Locate and identify every blood parasite.
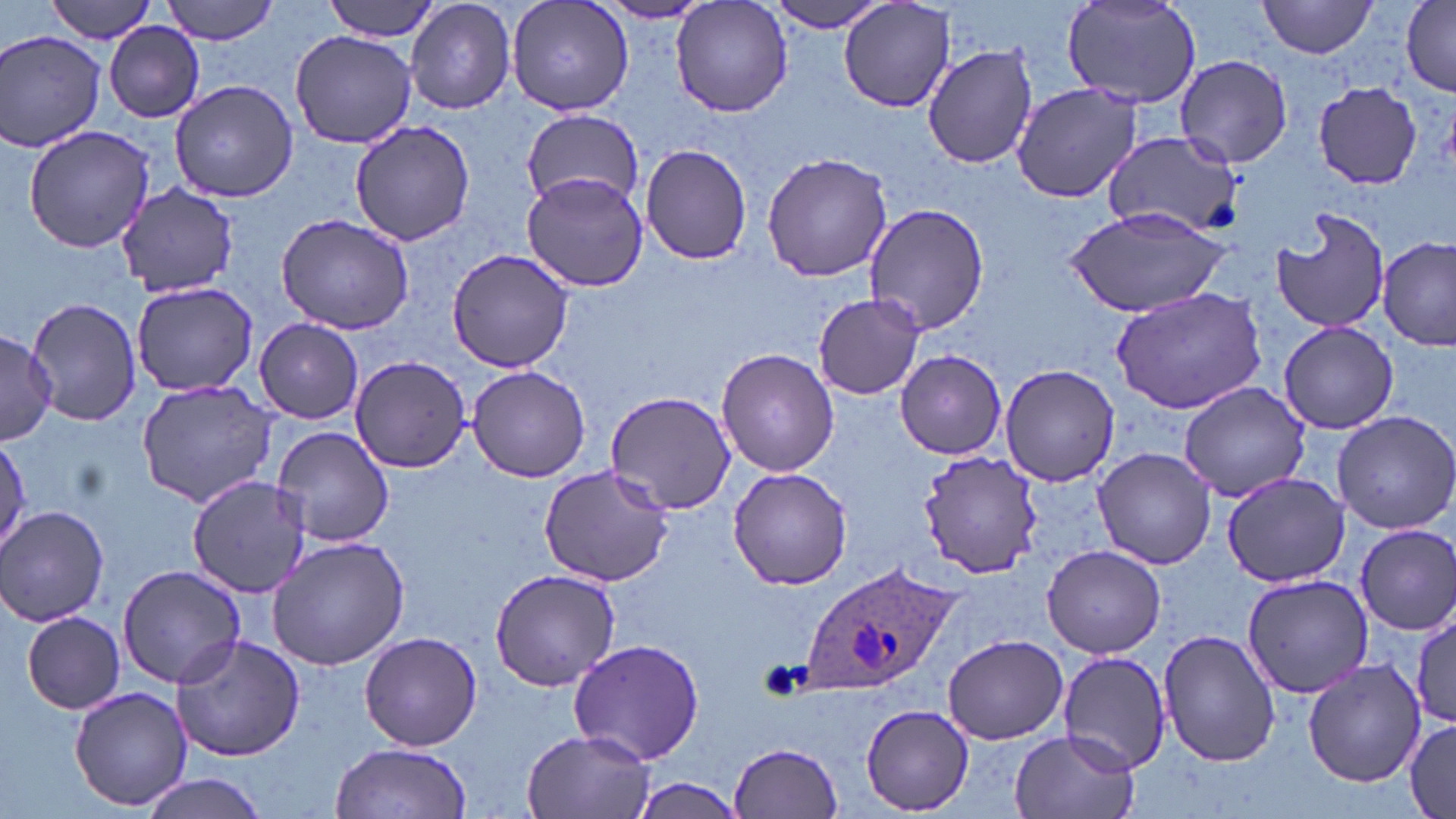
Approximate bounding boxes as named x1/y1/x2/y2 corners in pixels.
Plasmodium ovale-infected red blood cells: (x1=799, y1=560, x2=961, y2=696).
No Plasmodium falciparum, Plasmodium malariae, Plasmodium vivax, Babesia divergens, or Trypanosoma brucei observed.

Uninfected red blood cell locations: (x1=42, y1=0, x2=158, y2=42), (x1=160, y1=0, x2=284, y2=44), (x1=319, y1=0, x2=439, y2=43), (x1=507, y1=0, x2=634, y2=118), (x1=669, y1=0, x2=794, y2=119), (x1=1061, y1=0, x2=1203, y2=110), (x1=1258, y1=0, x2=1383, y2=59), (x1=406, y1=1, x2=517, y2=114), (x1=594, y1=1, x2=715, y2=23), (x1=766, y1=1, x2=889, y2=33), (x1=1401, y1=1, x2=1456, y2=94), (x1=840, y1=2, x2=958, y2=112), (x1=104, y1=21, x2=206, y2=122), (x1=290, y1=29, x2=416, y2=150), (x1=1, y1=31, x2=106, y2=154), (x1=923, y1=43, x2=1039, y2=169), (x1=1173, y1=54, x2=1293, y2=168), (x1=170, y1=78, x2=299, y2=203), (x1=1011, y1=82, x2=1141, y2=203), (x1=1314, y1=82, x2=1423, y2=189), (x1=518, y1=109, x2=646, y2=209), (x1=351, y1=120, x2=476, y2=245), (x1=23, y1=127, x2=154, y2=254), (x1=1101, y1=132, x2=1247, y2=238), (x1=641, y1=143, x2=752, y2=265), (x1=761, y1=151, x2=892, y2=282), (x1=521, y1=172, x2=650, y2=293), (x1=118, y1=184, x2=240, y2=296), (x1=864, y1=203, x2=988, y2=336), (x1=1270, y1=206, x2=1390, y2=334), (x1=1065, y1=208, x2=1234, y2=319), (x1=275, y1=212, x2=416, y2=334), (x1=1378, y1=238, x2=1455, y2=349), (x1=446, y1=247, x2=575, y2=374), (x1=130, y1=281, x2=260, y2=397), (x1=1111, y1=283, x2=1269, y2=414), (x1=814, y1=293, x2=926, y2=400), (x1=26, y1=297, x2=143, y2=429), (x1=255, y1=320, x2=364, y2=423), (x1=1278, y1=321, x2=1399, y2=435), (x1=0, y1=331, x2=55, y2=443), (x1=717, y1=349, x2=839, y2=476), (x1=895, y1=351, x2=1006, y2=459), (x1=349, y1=355, x2=473, y2=473), (x1=466, y1=364, x2=591, y2=483), (x1=1000, y1=364, x2=1120, y2=486), (x1=136, y1=380, x2=276, y2=506), (x1=1178, y1=382, x2=1312, y2=499), (x1=604, y1=391, x2=737, y2=516), (x1=1333, y1=410, x2=1456, y2=534), (x1=272, y1=425, x2=396, y2=549), (x1=0, y1=437, x2=31, y2=548), (x1=1092, y1=447, x2=1215, y2=570), (x1=919, y1=452, x2=1043, y2=578), (x1=538, y1=463, x2=675, y2=588), (x1=728, y1=466, x2=852, y2=591), (x1=1220, y1=470, x2=1351, y2=587), (x1=186, y1=475, x2=311, y2=599), (x1=0, y1=505, x2=113, y2=625), (x1=1353, y1=524, x2=1456, y2=635), (x1=267, y1=533, x2=409, y2=670), (x1=1042, y1=544, x2=1167, y2=657), (x1=115, y1=563, x2=245, y2=687), (x1=489, y1=568, x2=621, y2=691), (x1=1241, y1=573, x2=1375, y2=699), (x1=1412, y1=608, x2=1456, y2=732), (x1=19, y1=612, x2=127, y2=712), (x1=1159, y1=630, x2=1281, y2=768), (x1=359, y1=632, x2=484, y2=751), (x1=943, y1=634, x2=1068, y2=745), (x1=170, y1=635, x2=306, y2=762), (x1=569, y1=637, x2=704, y2=765), (x1=1056, y1=650, x2=1172, y2=774), (x1=1304, y1=660, x2=1425, y2=786), (x1=69, y1=687, x2=190, y2=811), (x1=861, y1=705, x2=974, y2=815), (x1=1403, y1=716, x2=1456, y2=819), (x1=520, y1=729, x2=657, y2=819), (x1=1009, y1=729, x2=1138, y2=819), (x1=729, y1=742, x2=845, y2=818), (x1=329, y1=743, x2=473, y2=819), (x1=135, y1=772, x2=273, y2=818), (x1=626, y1=780, x2=749, y2=819). Slide-level diagnosis: Plasmodium ovale. Thin blood smear. May-Grünwald-Giemsa stain. Captured at 1000x magnification. Optical microscopy. Image is 1456×819 pixels. One field of a larger specimen.